Describe the morphology of the erythrocytes.
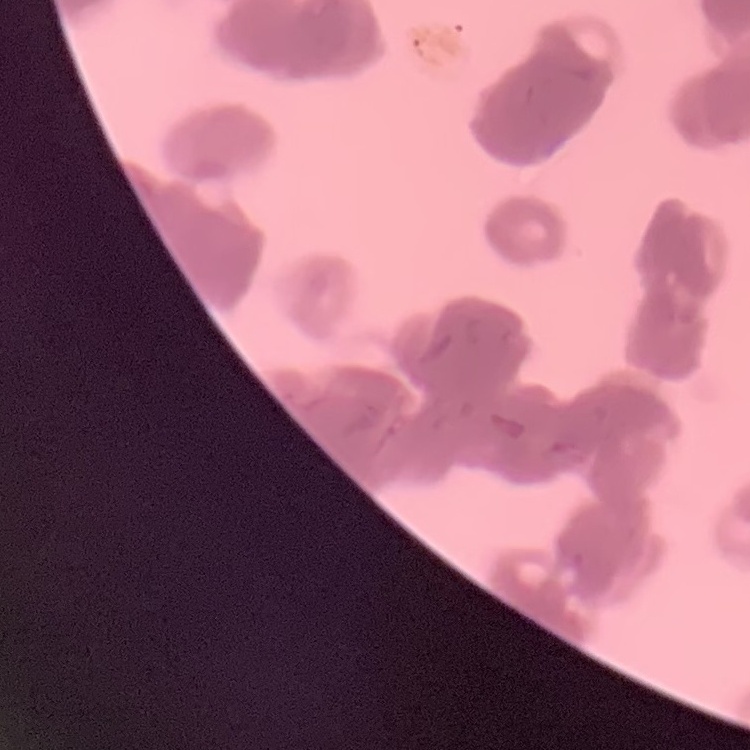
They show rouleaux formation.

Thin blood smear. Square crop of a larger photomicrograph. Stained with either Field's or Giemsa.